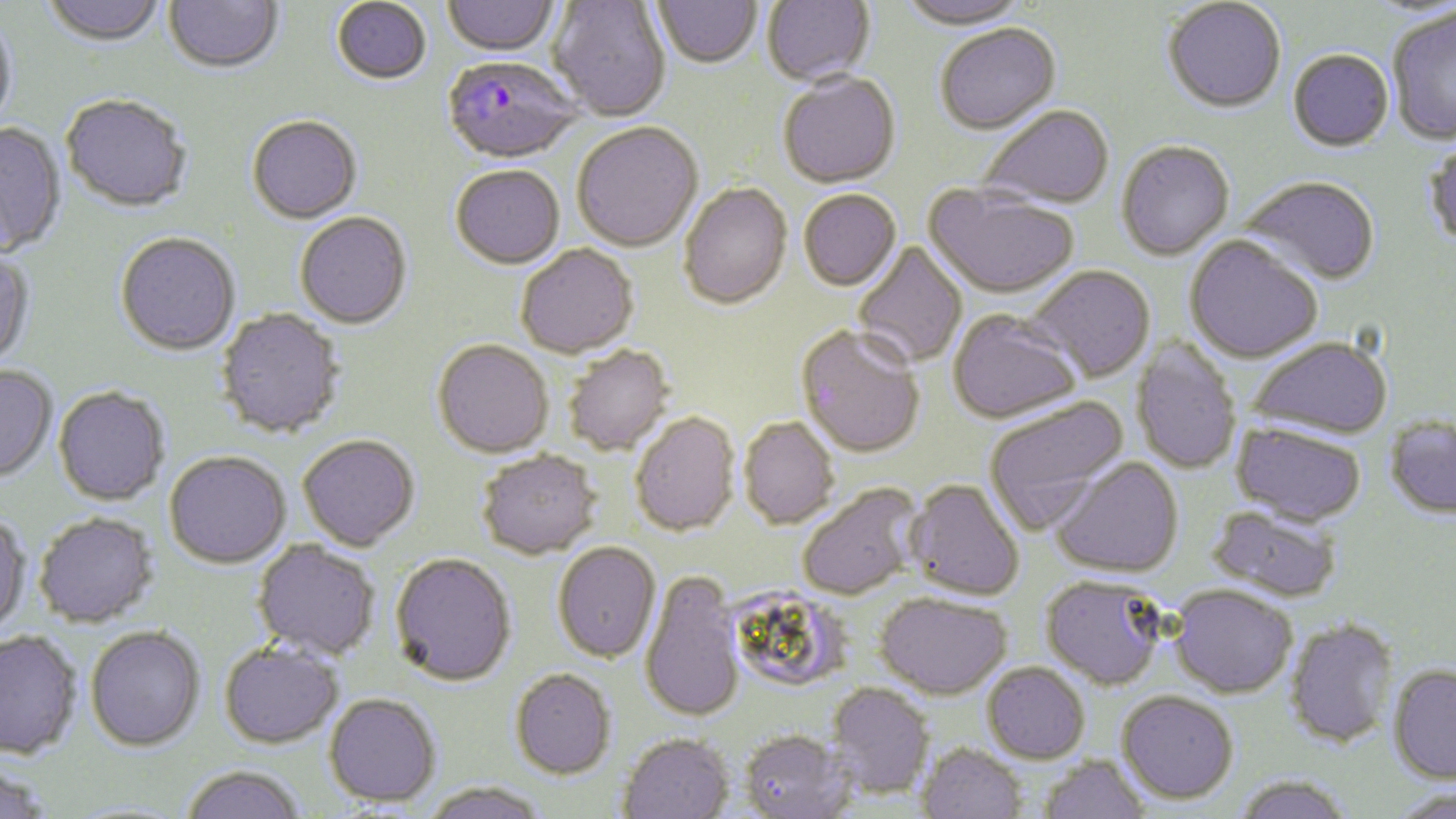

Summary:
  - Coordinate format: approximate bounding boxes as (x1,y1)-(x2,y2) corner pairs in pixels
  - Plasmodium falciparum-infected red blood cell locations: (441,59)-(585,166)
  - Uninfected red blood cell locations: (40,0)-(169,50), (164,0)-(284,77), (443,0)-(560,59), (548,0)-(671,123), (652,0)-(763,72), (762,0)-(876,88), (896,0)-(1032,32), (332,1)-(431,87), (1163,1)-(1286,114), (1387,6)-(1456,145), (0,13)-(18,138), (935,26)-(1061,137), (1288,49)-(1395,152), (777,74)-(901,190), (60,97)-(192,215), (978,107)-(1114,212), (246,117)-(362,226), (0,123)-(66,259), (572,125)-(702,254), (1422,139)-(1456,251), (1116,143)-(1234,262), (450,167)-(565,271), (1241,176)-(1380,286), (678,184)-(793,311), (924,185)-(1079,301), (798,191)-(902,292), (295,213)-(412,331), (115,233)-(241,357), (1184,236)-(1322,364), (852,241)-(968,368), (515,245)-(639,360), (0,250)-(35,372), (1027,265)-(1155,383), (215,308)-(346,438), (947,309)-(1083,424), (795,325)-(925,457), (1248,334)-(1393,439), (1130,338)-(1242,474), (432,340)-(553,458), (563,345)-(675,456), (0,365)-(57,483), (53,386)-(170,506), (984,397)-(1129,534), (630,412)-(740,537), (1383,415)-(1456,519), (739,417)-(839,528), (1231,422)-(1367,525), (298,434)-(420,550), (477,449)-(602,559), (164,451)-(291,568), (1050,457)-(1184,577), (905,479)-(1025,600), (796,483)-(923,600), (1207,504)-(1344,603), (0,512)-(31,636), (34,512)-(159,627), (253,540)-(380,660), (552,542)-(660,662), (390,552)-(517,686), (641,570)-(745,723), (1041,575)-(1167,689), (1170,584)-(1298,698), (723,590)-(850,687), (874,592)-(1012,699), (1285,617)-(1399,748), (85,625)-(206,751), (0,630)-(83,759), (219,641)-(344,748), (982,662)-(1090,763), (1387,664)-(1456,784), (509,668)-(616,779), (827,682)-(934,798), (1116,690)-(1239,803), (324,693)-(442,807), (740,730)-(854,819), (617,733)-(734,819), (918,742)-(1027,819), (1037,754)-(1151,819), (0,758)-(54,819), (180,764)-(307,819), (1232,774)-(1357,819), (422,780)-(549,819), (1387,787)-(1456,819)
  - Slide-level diagnosis: Plasmodium falciparum
  - Image size: 1456×819 pixels
  - Magnification: 1000x
  - Field of view: single
  - Preparation: thin blood smear
  - Stain: May-Grünwald-Giemsa
  - Modality: light microscopy